Assess this cell for malaria.
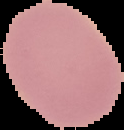

Uninfected.

Summary:
  - Preparation: thin blood smear
  - Image type: segmented cell region on a black background
  - Image size: 124×130 pixels